Identify the parasite.
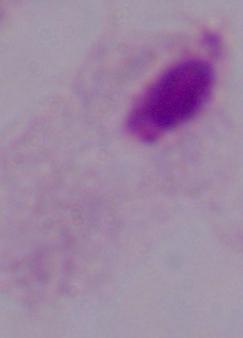
A trichomonad.

{
  "magnification": "1000x",
  "modality": "photomicrograph"
}